Assess this cell for malaria.
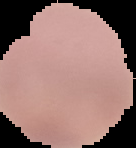
Uninfected.

Summary:
  - Image type: cell region segmented out of the field of view; surrounding area masked to black
  - Image size: 136×148 pixels
  - Preparation: thin blood film